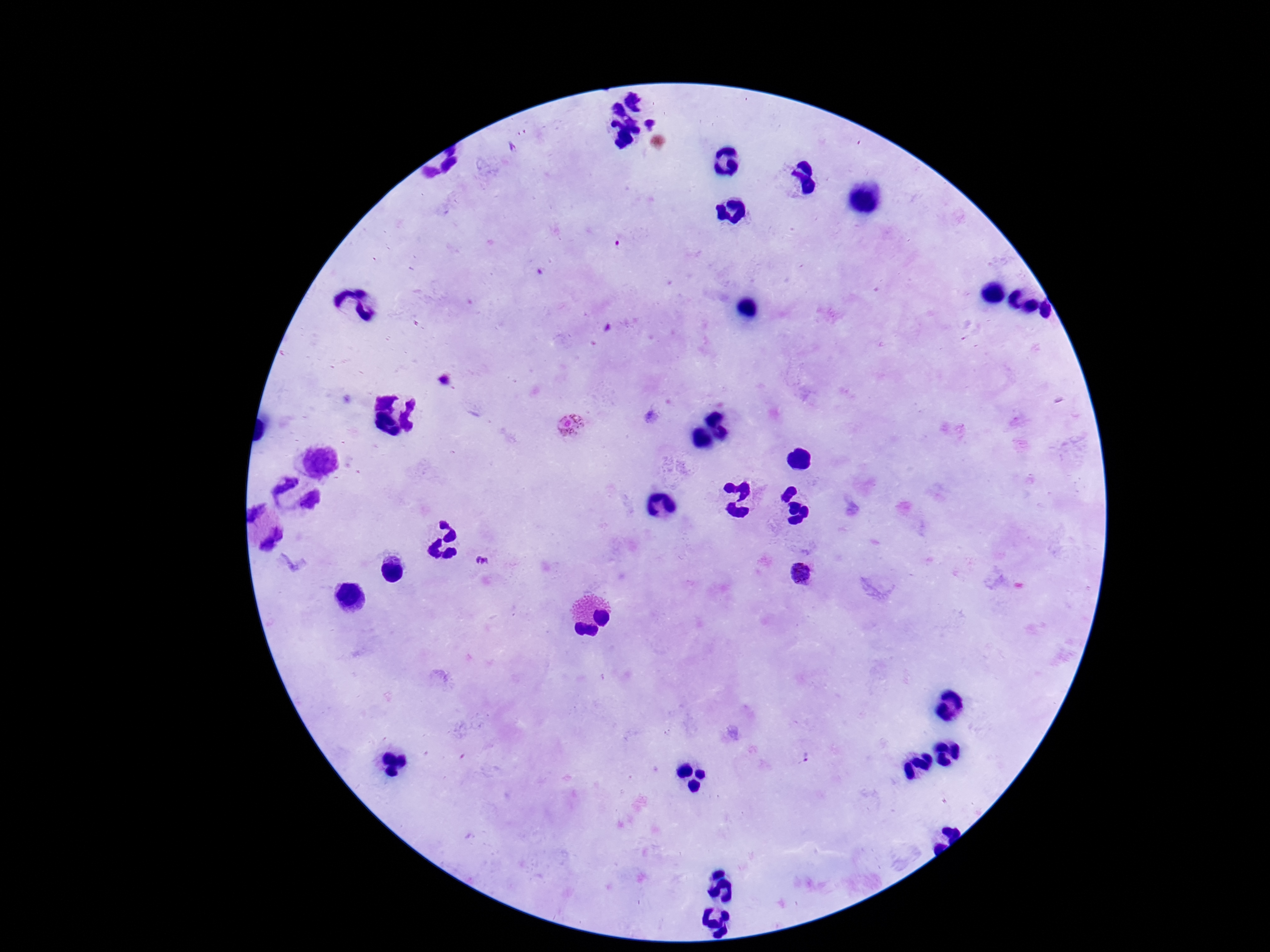 Approximate centers as [x, y] in pixels. Plasmodium parasite locations: [570, 426], [480, 562]. Single field of view. Giemsa-stained preparation. Image is 1270×952 pixels. 100x magnification. Smartphone photograph taken through the microscope eyepiece. Patient malaria status: infected. Thick peripheral-blood smear.